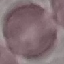 Result: negative for malaria parasites. Thin blood film. Photographed with a smartphone camera at the microscope eyepiece. Giemsa-stained preparation. Cell patch, automatically extracted from a larger field of view and resized to 64 × 64 pixels.